Assess the morphology of the red blood cells.
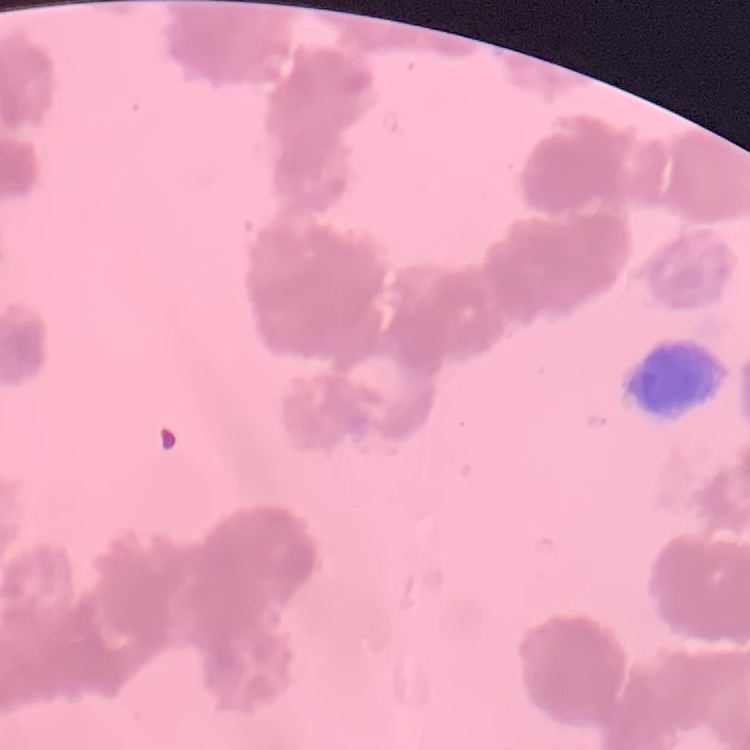

They show rouleaux formation.

image type = one tile cut from a larger photomicrograph
stain = Field's or Giemsa
preparation = thin blood film